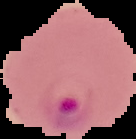
preparation = thin blood film
image type = segmented cell region on a black background
malaria status = parasitized
image size = 136×139 pixels